Outline each Plasmodium vivax-infected red blood cell.
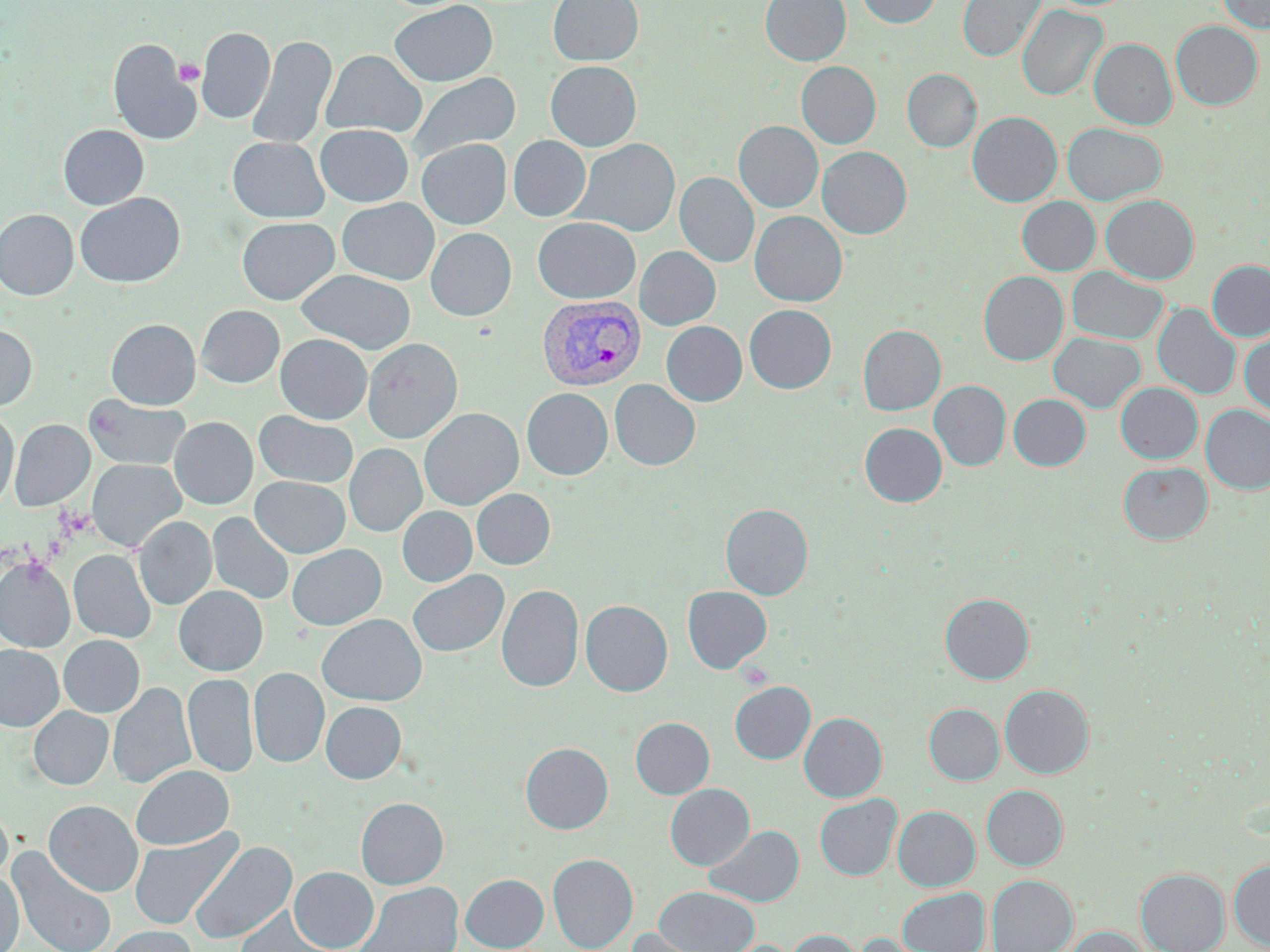
Approximate bounding boxes as (x1, y1, x2, y2) in pixels.
Plasmodium vivax-infected red blood cells: (537, 295, 646, 391).

slide-level diagnosis = Plasmodium vivax
uninfected red blood cell locations = approximate bounding boxes as (x1, y1, x2, y2) in pixels: (548, 0, 643, 66), (761, 0, 851, 65), (857, 0, 941, 28), (957, 0, 1046, 62), (1218, 0, 1270, 34), (390, 1, 497, 87), (1017, 5, 1107, 101), (1171, 21, 1262, 110), (196, 26, 275, 124), (246, 35, 336, 149), (108, 39, 201, 145), (1090, 39, 1176, 129), (321, 50, 426, 138), (546, 61, 641, 151), (796, 61, 881, 149), (902, 69, 981, 152), (407, 72, 520, 162), (967, 112, 1062, 207), (734, 121, 823, 212), (1062, 123, 1167, 205), (315, 124, 413, 207), (58, 125, 148, 210), (508, 136, 591, 221), (228, 137, 328, 223), (572, 138, 680, 237), (417, 139, 511, 229), (817, 146, 912, 239), (675, 172, 759, 267), (75, 193, 185, 288), (1101, 195, 1199, 284), (1017, 196, 1100, 275), (337, 198, 439, 285), (0, 209, 78, 300), (750, 211, 847, 306), (237, 217, 339, 305), (533, 217, 640, 303), (426, 228, 516, 321), (635, 246, 720, 330), (1207, 260, 1270, 341), (1067, 266, 1169, 345), (296, 269, 415, 354), (979, 271, 1068, 365), (1153, 303, 1241, 400), (744, 304, 836, 393), (196, 305, 284, 387), (106, 319, 201, 409), (661, 321, 747, 406), (0, 324, 36, 411), (858, 325, 945, 415), (1239, 330, 1270, 417), (1048, 332, 1145, 413), (275, 334, 371, 424), (362, 338, 463, 443), (610, 380, 700, 470), (929, 380, 1010, 471), (1116, 383, 1202, 463), (522, 387, 612, 479), (1009, 394, 1091, 470), (85, 396, 190, 471), (1200, 404, 1270, 494), (419, 408, 523, 510), (0, 409, 18, 510), (253, 411, 358, 488), (169, 417, 257, 509), (9, 419, 94, 511), (860, 423, 946, 507), (344, 444, 426, 536), (87, 459, 185, 553), (1119, 462, 1212, 544), (251, 477, 350, 557), (471, 488, 555, 569), (721, 504, 812, 599), (397, 506, 477, 586), (208, 512, 294, 605), (134, 516, 216, 610), (287, 544, 386, 630), (68, 550, 155, 643), (0, 558, 74, 652), (407, 570, 509, 658), (497, 584, 583, 692), (174, 585, 267, 675), (682, 586, 772, 673), (940, 593, 1034, 684), (581, 600, 672, 696), (317, 614, 426, 705), (58, 634, 144, 717), (0, 645, 63, 731), (249, 667, 329, 768), (182, 672, 258, 778), (730, 681, 815, 764), (108, 682, 195, 789), (999, 685, 1094, 778), (321, 701, 406, 783), (924, 704, 1003, 784), (28, 706, 113, 789), (799, 712, 887, 802), (630, 717, 715, 799), (520, 742, 613, 834), (132, 765, 234, 850), (664, 783, 755, 870), (981, 785, 1068, 870), (814, 794, 902, 880), (356, 798, 448, 889), (43, 800, 143, 896), (0, 801, 13, 884), (893, 805, 980, 891), (704, 825, 804, 907), (128, 828, 242, 930), (190, 841, 296, 944), (7, 847, 117, 952), (548, 853, 638, 952), (1229, 859, 1270, 951), (289, 867, 378, 951), (1136, 868, 1230, 952), (0, 871, 24, 952), (461, 874, 548, 951), (986, 875, 1077, 952), (355, 882, 463, 952), (653, 886, 759, 952), (897, 887, 990, 952), (234, 907, 339, 952), (105, 926, 197, 952), (1062, 926, 1149, 952), (626, 928, 716, 952), (784, 929, 863, 952), (853, 933, 941, 952)
modality = optical microscopy
magnification = 1000x
preparation = thin blood smear
image size = 1270×952 pixels
field of view = one of a larger specimen
stain = May-Grünwald-Giemsa
platelet locations = approximate bounding boxes as (x1, y1, x2, y2) in pixels: (174, 59, 204, 86)